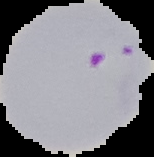
Segmented cell region on a black background. Malaria status: parasitized. From a thin blood film. Image is 154×157 pixels.